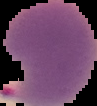

preparation = thin blood film
image size = 97×106 pixels
image type = cell region segmented out of the field of view; surrounding area masked to black
malaria status = parasitized